Report the malaria status of this cell.
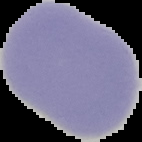
It is uninfected.

preparation = thin blood film
image size = 142×142 pixels
image type = segmented cell region on a black background